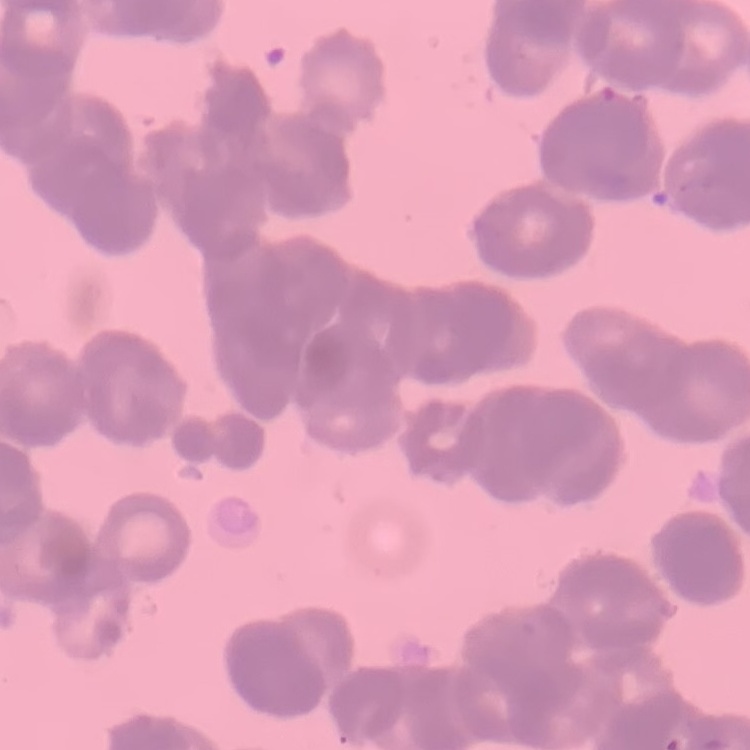

{
  "erythrocyte_morphology": "rouleaux formation",
  "stain": "Field's or Giemsa",
  "preparation": "thin peripheral smear",
  "image_type": "square crop of a larger photomicrograph"
}